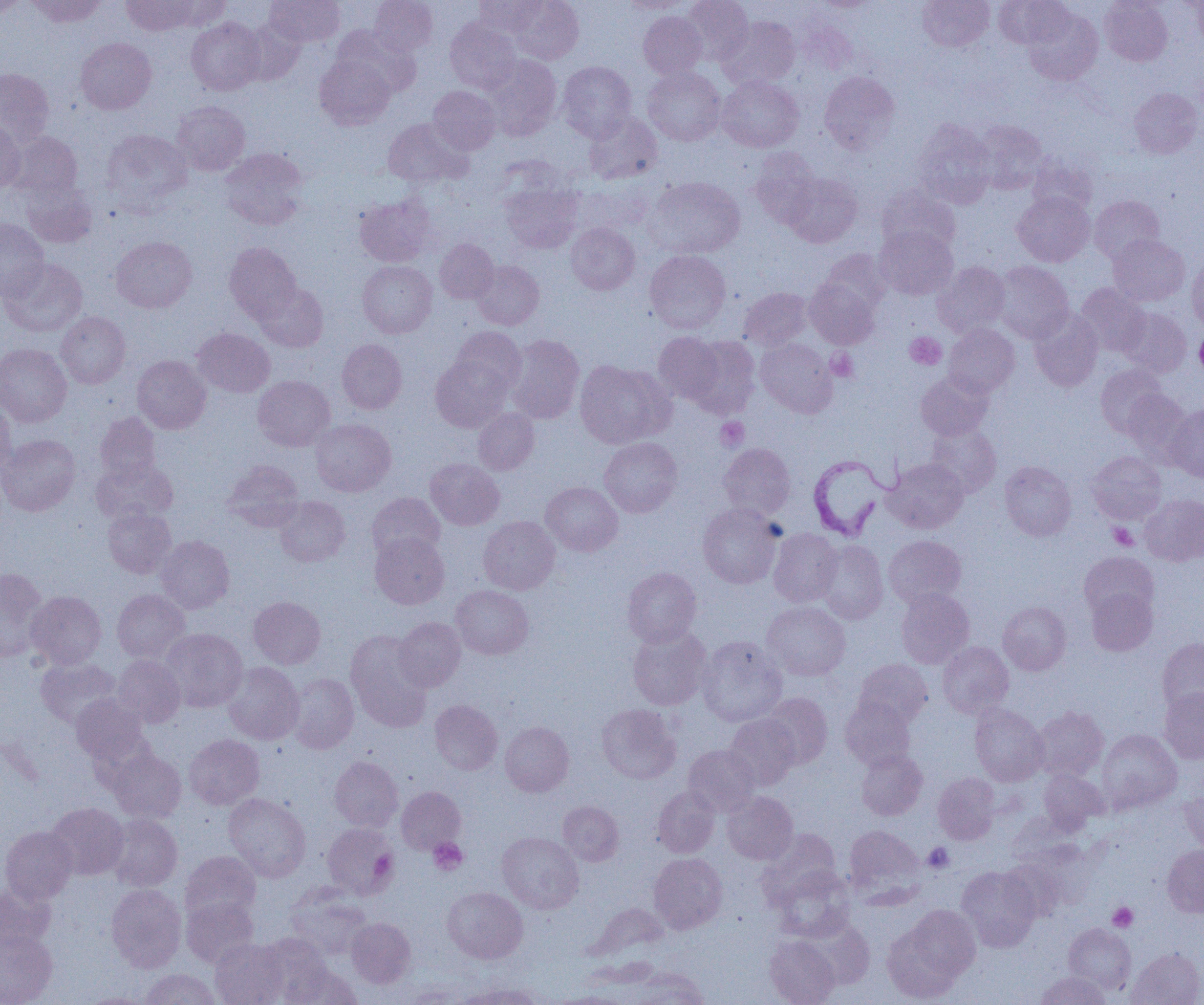
Summary:
  - Coordinate format: approximate bounding boxes as (x1,y1)-(x2,y2) corner pairs in pixels
  - Uninfected red blood cell locations: (27,0)-(105,27), (122,0)-(195,36), (164,0)-(231,30), (265,0)-(345,47), (370,0)-(438,56), (474,0)-(545,37), (509,0)-(584,64), (619,0)-(692,13), (681,0)-(753,65), (917,0)-(994,51), (994,0)-(1072,48), (1100,0)-(1172,66), (0,1)-(28,18), (811,1)-(879,13), (1191,1)-(1204,49), (1023,7)-(1102,85), (638,12)-(707,79), (718,16)-(800,89), (186,17)-(265,95), (445,18)-(521,93), (241,19)-(304,84), (797,20)-(858,74), (331,26)-(420,95), (76,37)-(156,114), (483,54)-(562,140), (315,55)-(395,129), (557,61)-(636,140), (643,67)-(725,145), (0,69)-(54,146), (819,71)-(900,154), (717,75)-(803,152), (428,86)-(500,154), (1129,87)-(1202,158), (172,101)-(250,175), (585,112)-(662,183), (383,118)-(469,188), (0,119)-(25,192), (912,120)-(995,208), (973,120)-(1047,193), (101,128)-(193,212), (8,131)-(82,199), (220,148)-(308,230), (750,149)-(822,227), (1027,154)-(1098,216), (783,172)-(862,247), (645,176)-(745,258), (22,180)-(97,248), (500,182)-(583,253), (877,185)-(960,254), (1013,191)-(1094,266), (355,195)-(435,266), (1089,195)-(1164,263), (0,218)-(49,301), (566,223)-(639,294), (874,226)-(958,299), (1109,234)-(1190,305), (111,236)-(197,313), (435,239)-(498,303), (225,242)-(301,322), (819,249)-(890,314), (645,250)-(731,333), (1,257)-(87,336), (1187,257)-(1204,331), (358,260)-(437,338), (471,260)-(544,329), (993,261)-(1073,343), (933,262)-(1011,338), (805,278)-(879,348), (255,283)-(328,352), (1075,283)-(1149,356), (739,287)-(812,350), (1118,307)-(1192,377), (1029,308)-(1103,391), (56,311)-(130,388), (943,324)-(1019,397), (192,327)-(275,397), (451,327)-(526,396), (654,332)-(726,405), (505,334)-(584,423), (685,335)-(760,417), (756,338)-(837,417), (337,339)-(407,413), (0,344)-(71,426), (132,355)-(211,433), (430,355)-(512,432), (574,360)-(673,448), (1095,364)-(1168,436), (916,372)-(992,440), (253,375)-(335,450), (1123,391)-(1192,460), (0,399)-(16,476), (1166,404)-(1204,481), (473,407)-(539,474), (95,412)-(160,483), (310,418)-(396,496), (925,425)-(1001,497), (0,434)-(80,516), (599,437)-(682,517), (718,443)-(796,520), (1087,451)-(1166,523), (425,458)-(504,530), (883,458)-(968,533), (91,459)-(177,524), (222,460)-(304,532), (1000,461)-(1076,540), (541,481)-(623,556), (366,492)-(445,561), (1140,494)-(1204,565), (275,496)-(350,566), (697,503)-(782,588), (103,506)-(176,578), (478,516)-(560,594), (769,528)-(842,606), (370,531)-(449,609), (156,535)-(234,613), (884,535)-(966,608), (814,540)-(888,624), (1079,552)-(1158,621), (623,567)-(701,647), (0,568)-(48,662), (450,585)-(534,659), (896,588)-(974,668), (1086,588)-(1158,655), (112,589)-(191,662), (27,591)-(106,668), (249,596)-(325,669), (762,601)-(851,681), (998,602)-(1071,675), (394,617)-(466,691), (628,625)-(712,710), (161,628)-(248,712), (345,630)-(432,730), (697,636)-(787,727), (1157,638)-(1204,716), (937,641)-(1014,718), (113,655)-(186,726), (36,657)-(121,728), (854,658)-(932,728), (223,662)-(303,744), (287,673)-(359,753), (1160,688)-(1204,762), (761,693)-(832,768), (71,694)-(149,765), (840,697)-(916,770), (429,699)-(502,774), (597,704)-(681,784), (970,704)-(1048,785), (1032,706)-(1108,781), (725,714)-(799,789), (500,721)-(573,796), (1097,729)-(1182,813), (184,734)-(264,809), (684,744)-(760,816), (108,749)-(186,822), (856,749)-(927,820), (329,756)-(403,831), (1038,770)-(1108,832), (933,772)-(1000,844), (396,786)-(466,854), (653,786)-(720,857), (1179,788)-(1204,854), (722,791)-(797,864), (223,793)-(311,881), (558,801)-(623,866), (47,803)-(128,879), (106,813)-(183,891), (322,823)-(400,899), (844,825)-(925,902), (0,826)-(77,904), (757,829)-(841,905), (497,832)-(583,913), (1162,845)-(1204,917), (180,851)-(261,925), (649,853)-(727,933), (999,857)-(1067,921), (957,866)-(1040,952), (772,867)-(855,941), (0,884)-(54,954), (106,884)-(186,972), (285,885)-(372,959), (442,887)-(527,963), (181,897)-(258,968), (897,904)-(981,987), (347,917)-(415,988), (805,918)-(875,989), (1064,923)-(1136,994), (0,929)-(57,1005), (256,934)-(332,1000), (765,935)-(840,1005), (210,939)-(289,1005), (1127,948)-(1204,1005), (284,963)-(361,1005), (624,966)-(710,1004), (140,969)-(222,1005), (1035,970)-(1111,1004), (451,982)-(545,1005), (549,991)-(635,1005), (81,992)-(153,1005)
  - Trypanosoma brucei locations: (807,452)-(899,541)
  - Platelet locations: (905,332)-(946,370), (826,348)-(858,381), (716,417)-(749,451), (1109,523)-(1138,550), (428,837)-(467,875), (923,842)-(954,874), (370,850)-(397,877), (1108,902)-(1138,931)
  - Slide-level diagnosis: Trypanosoma brucei
  - Magnification: 1000x
  - Field of view: one of a larger specimen
  - Modality: optical microscopy
  - Image size: 1204×1005 pixels
  - Preparation: thin blood smear